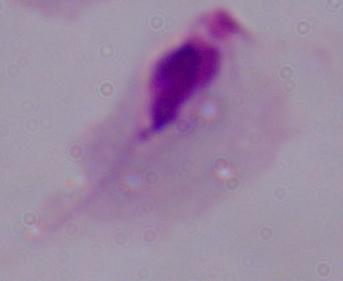
modality = micrograph
identification = trichomonad
magnification = 1000x